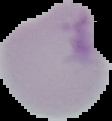
image size = 112×121 pixels
malaria status = uninfected
image type = cell region segmented out of the field of view; surrounding area masked to black
preparation = thin blood film